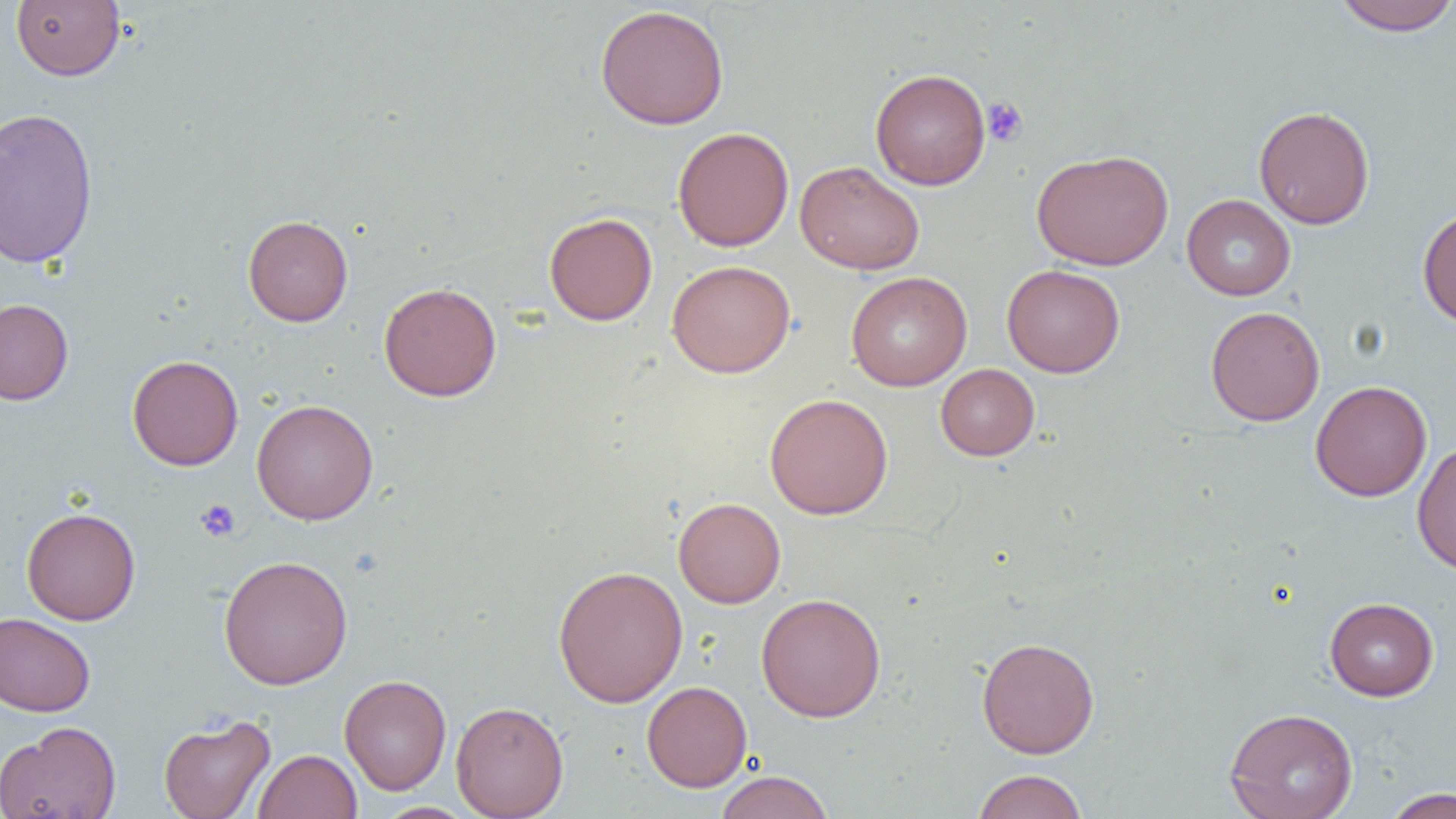
Summary:
  - Coordinate format: approximate bounding boxes as (x1, y1, x2, y2) in pixels
  - Uninfected red blood cell locations: (11, 0, 125, 81), (1332, 0, 1455, 36), (595, 4, 730, 130), (870, 68, 991, 190), (1254, 105, 1375, 230), (0, 106, 99, 268), (672, 126, 793, 252), (1031, 149, 1174, 270), (795, 160, 925, 275), (1182, 194, 1296, 300), (1417, 206, 1456, 328), (544, 212, 658, 325), (242, 214, 353, 326), (667, 260, 795, 378), (1002, 264, 1125, 378), (846, 271, 972, 391), (378, 282, 502, 401), (0, 299, 73, 405), (1205, 305, 1325, 426), (127, 354, 243, 470), (935, 364, 1039, 461), (1310, 380, 1432, 502), (764, 393, 893, 519), (251, 399, 379, 525), (1412, 441, 1456, 575), (673, 497, 786, 608), (21, 507, 141, 625), (218, 554, 353, 690), (553, 565, 688, 708), (756, 592, 886, 722), (1324, 597, 1439, 701), (0, 612, 95, 716), (976, 636, 1100, 759), (339, 674, 452, 795), (642, 681, 752, 792), (451, 700, 568, 819), (1224, 707, 1358, 819), (158, 714, 275, 819), (0, 721, 122, 819), (253, 749, 362, 819), (971, 769, 1088, 819), (714, 770, 835, 819), (1384, 787, 1455, 818), (374, 802, 478, 819)
  - Platelet locations: (982, 96, 1029, 147), (195, 499, 240, 542)
  - Slide-level diagnosis: no evidence of blood parasites
  - Preparation: thin blood film
  - Modality: light microscopy
  - Magnification: 1000x
  - Field of view: one of a larger specimen
  - Image size: 1456×819 pixels